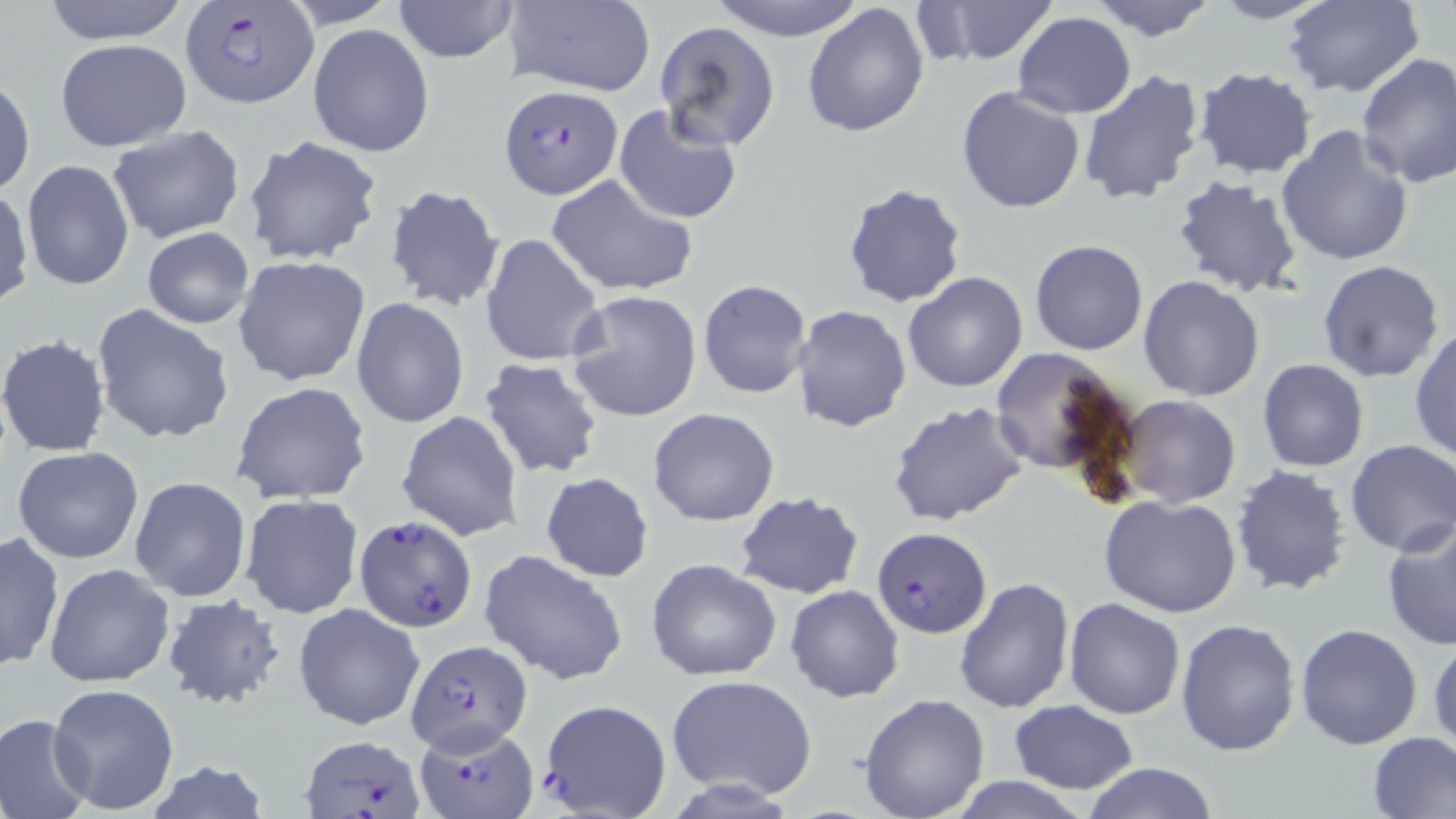
Summary:
  - Coordinate format: approximate bounding boxes as [x1, y1, x2, y2] in pixels
  - Plasmodium falciparum-infected red blood cell locations: [179, 4, 319, 107], [498, 85, 624, 200], [354, 517, 477, 632], [872, 527, 993, 639], [405, 639, 533, 755], [538, 699, 672, 818], [416, 721, 539, 818], [301, 735, 426, 817]
  - Uninfected red blood cell locations: [36, 0, 196, 45], [281, 0, 403, 29], [391, 0, 521, 63], [504, 0, 656, 96], [707, 0, 868, 42], [922, 0, 1057, 65], [1204, 0, 1336, 25], [1087, 1, 1222, 42], [1282, 1, 1427, 99], [803, 3, 930, 138], [1014, 11, 1136, 119], [655, 21, 781, 149], [308, 24, 435, 158], [54, 37, 192, 152], [1355, 53, 1456, 191], [1192, 68, 1317, 180], [1077, 69, 1207, 207], [0, 73, 35, 198], [956, 85, 1088, 213], [613, 105, 743, 225], [105, 125, 246, 243], [1276, 126, 1416, 267], [242, 135, 385, 266], [20, 159, 134, 292], [546, 174, 698, 300], [1170, 175, 1303, 299], [841, 182, 968, 307], [384, 184, 504, 312], [0, 186, 32, 310], [142, 227, 255, 329], [480, 232, 604, 368], [1028, 240, 1148, 356], [234, 257, 371, 388], [1316, 260, 1446, 384], [902, 271, 1029, 392], [1137, 276, 1266, 402], [698, 279, 813, 400], [565, 290, 702, 423], [351, 298, 469, 428], [91, 303, 234, 445], [789, 304, 912, 431], [1409, 326, 1456, 463], [0, 335, 111, 458], [988, 347, 1135, 482], [480, 358, 603, 479], [1258, 359, 1369, 472], [230, 381, 372, 505], [1117, 396, 1241, 509], [887, 398, 1031, 527], [647, 407, 780, 527], [396, 410, 525, 542], [1345, 438, 1456, 556], [13, 447, 144, 564], [1229, 464, 1354, 597], [540, 473, 654, 582], [130, 477, 251, 602], [239, 492, 363, 619], [735, 492, 863, 599], [1099, 495, 1245, 619], [1381, 519, 1456, 652], [1, 531, 62, 671], [479, 549, 629, 686], [646, 559, 784, 680], [43, 563, 175, 688], [953, 575, 1074, 713], [785, 585, 904, 701], [161, 594, 287, 711], [1063, 598, 1185, 720], [293, 602, 425, 731], [1175, 618, 1302, 758], [1296, 625, 1424, 749], [1428, 635, 1456, 750], [666, 675, 818, 799], [47, 682, 181, 815], [859, 693, 990, 817], [1010, 700, 1138, 793], [0, 714, 95, 819], [1366, 732, 1456, 818], [144, 762, 272, 818], [1080, 762, 1219, 819], [940, 777, 1097, 818]
  - Slide-level diagnosis: Plasmodium falciparum
  - Modality: light microscopy
  - Field of view: one of a larger specimen
  - Image size: 1456×819 pixels
  - Magnification: 1000x
  - Stain: May-Grünwald-Giemsa
  - Preparation: thin blood film